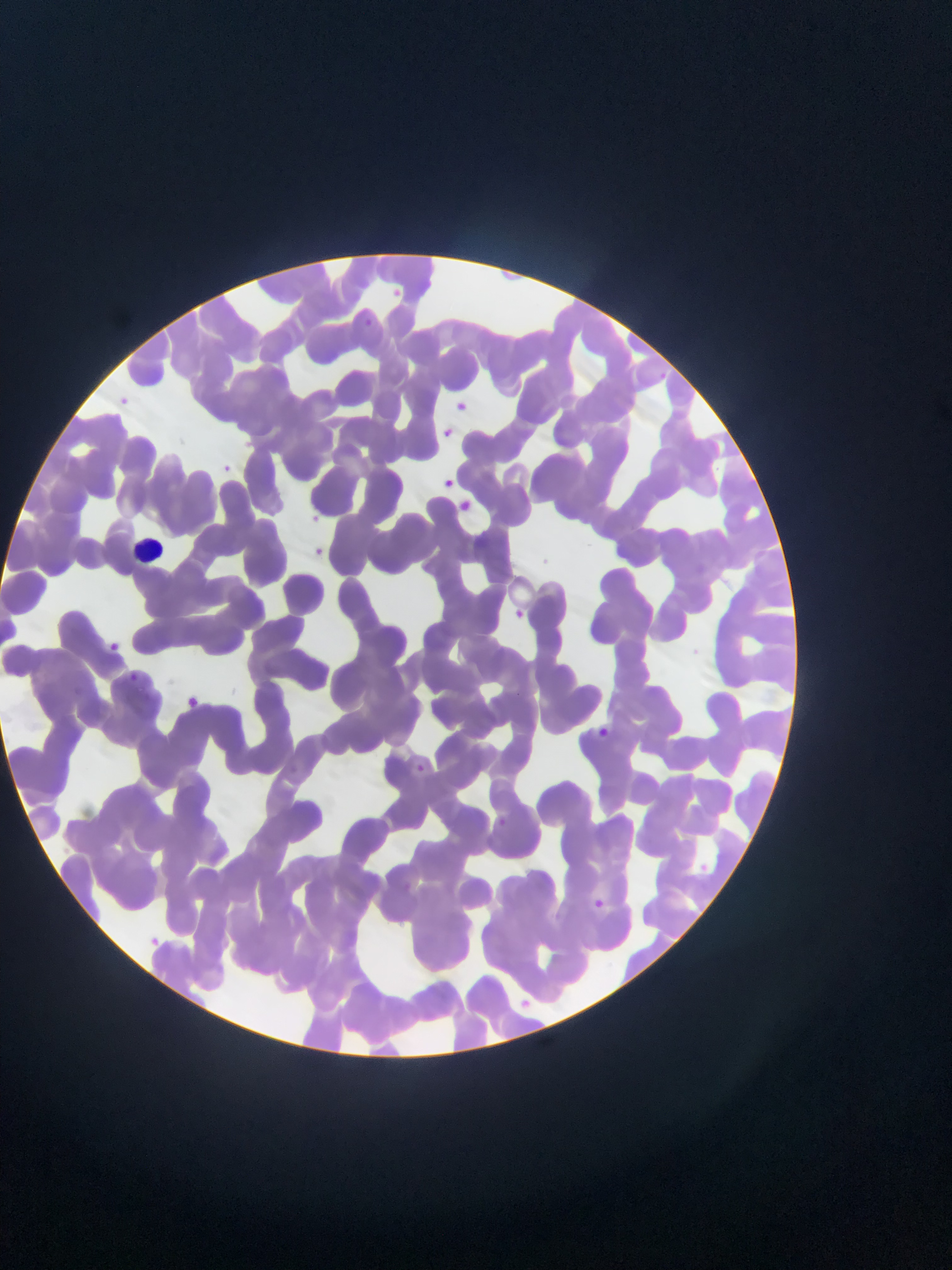
{
  "field_of_view": "single",
  "country": "Ghana",
  "capture": "mobile-phone photograph through a microscope",
  "image_size": "952×1270 pixels",
  "preparation": "thin blood film",
  "leukocyte_locations": "approximate bounding boxes as [left, top, right, bottom] in pixels: [134, 530, 184, 559]",
  "plasmodium_parasite_locations": "approximate bounding boxes as [left, top, right, bottom] in pixels: [389, 281, 409, 302], [363, 313, 377, 331], [658, 368, 671, 385], [118, 389, 143, 422], [452, 400, 480, 423], [436, 426, 449, 440], [222, 456, 241, 481], [441, 474, 458, 490], [462, 498, 475, 515], [303, 506, 321, 527], [313, 539, 335, 569], [516, 605, 533, 628], [107, 634, 127, 652], [130, 673, 138, 681], [188, 696, 202, 708], [595, 720, 612, 742], [412, 759, 432, 779], [497, 815, 506, 824], [597, 901, 607, 913], [145, 927, 164, 946]"
}